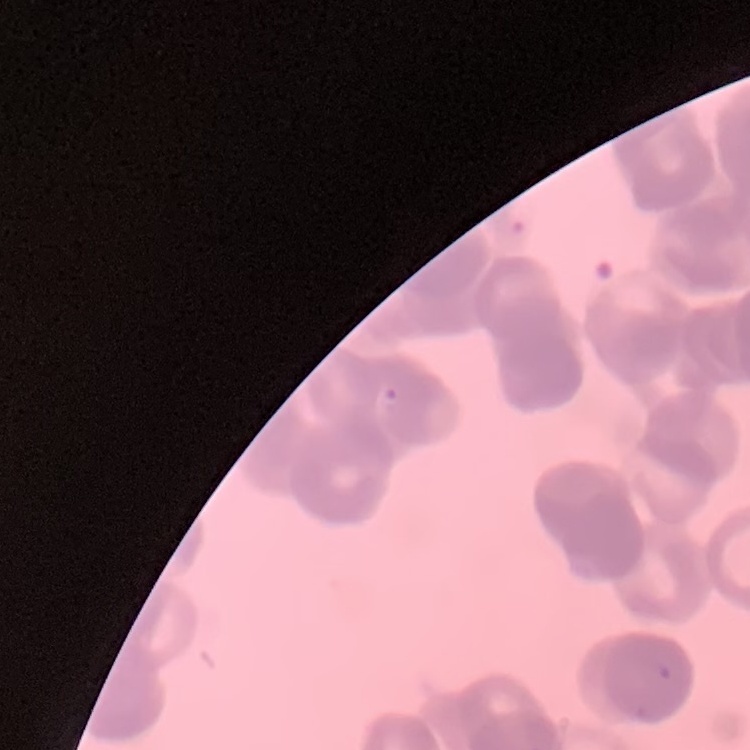

The erythrocytes exhibit rouleaux formation. Field's or Giemsa stain. Thin blood smear. Square crop of a larger photomicrograph.